Describe the morphology of the red blood cells.
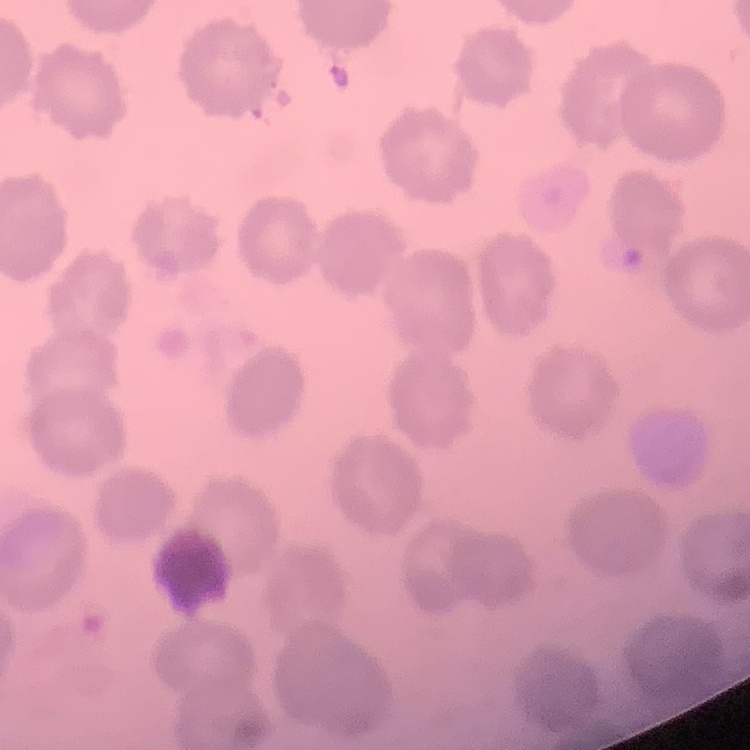

No rouleaux formation.

{
  "stain": "Field's or Giemsa",
  "image_type": "one tile cut from a larger photomicrograph",
  "preparation": "thin peripheral smear"
}